Assess for Plasmodium parasites.
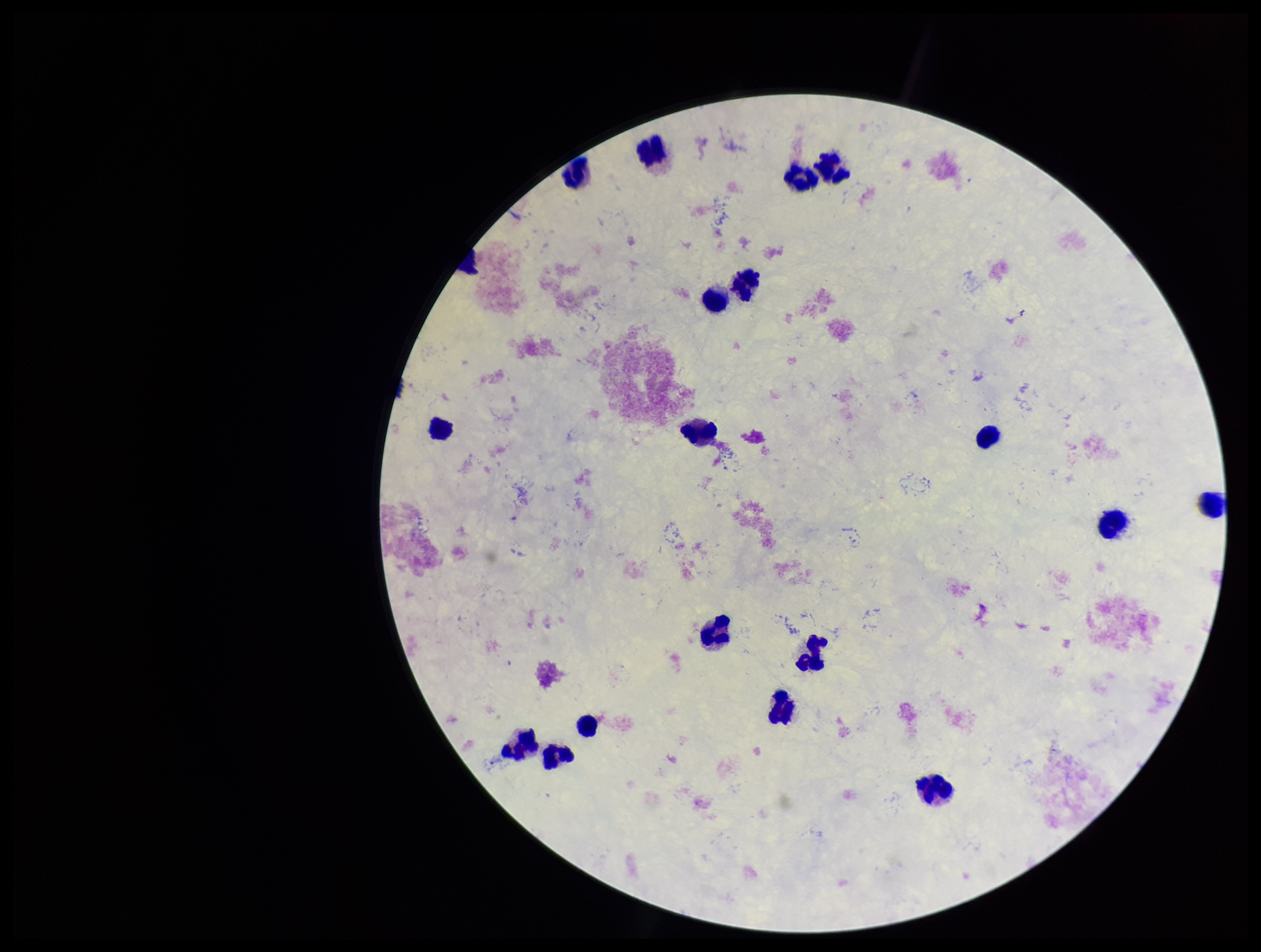
None detected.

patient malaria status = negative
field of view = single
parasite count = 0
leukocyte count = 19
capture = smartphone photograph through the microscope eyepiece
image size = 1261×952 pixels
stain = Giemsa
preparation = thick